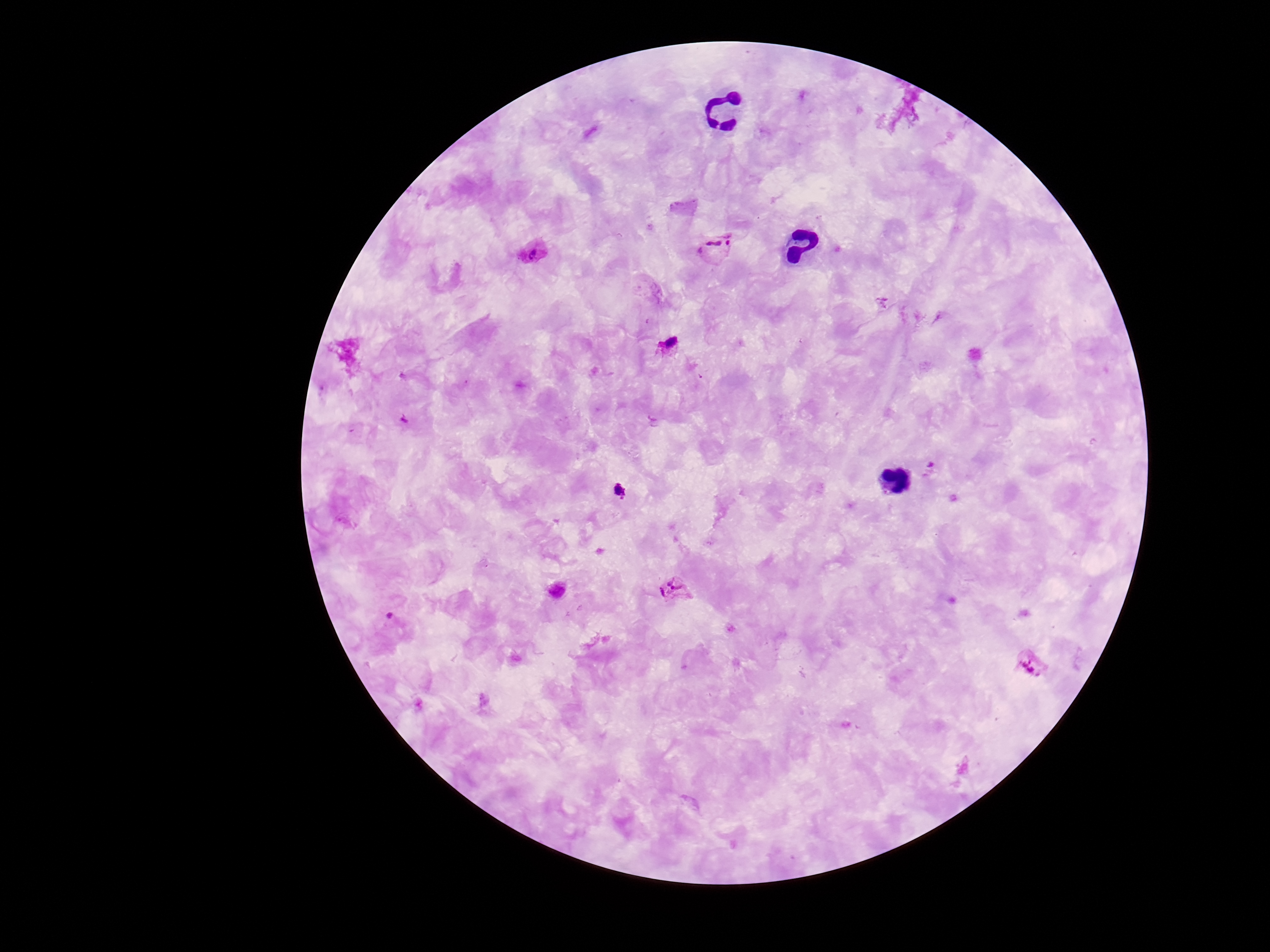
Approximate centers as [x, y] in pixels.
Summary:
  - Plasmodium parasite locations: [718, 249], [534, 253], [671, 348], [930, 470], [676, 592], [1028, 666]
  - Preparation: thick blood smear
  - Magnification: 100x
  - Image size: 1270×952 pixels
  - Patient malaria status: infected
  - Stain: Giemsa
  - Capture: smartphone camera through the microscope eyepiece
  - Field of view: single